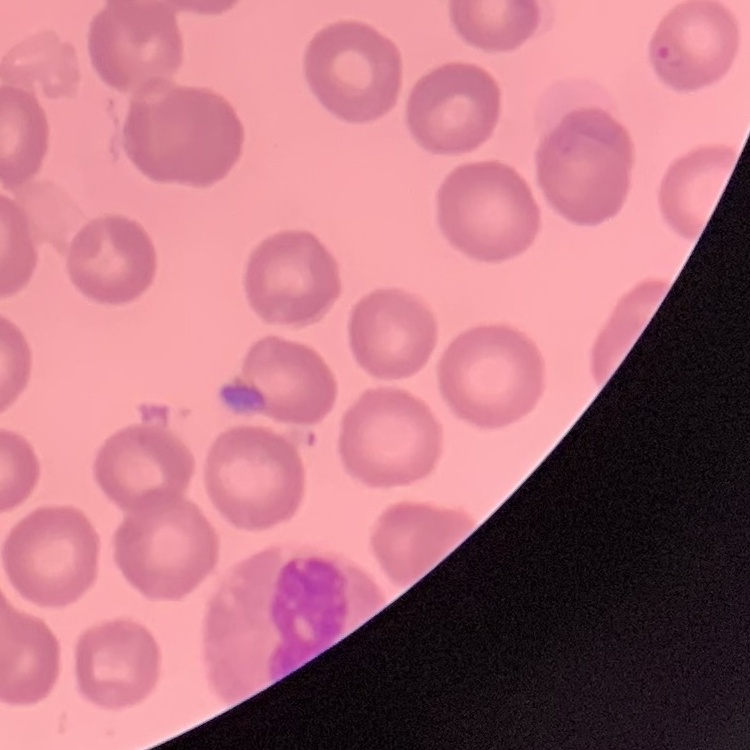
Summary:
  - Erythrocyte morphology: no rouleaux formation
  - Preparation: thin blood film
  - Image type: one tile cut from a larger photomicrograph
  - Stain: Field's or Giemsa